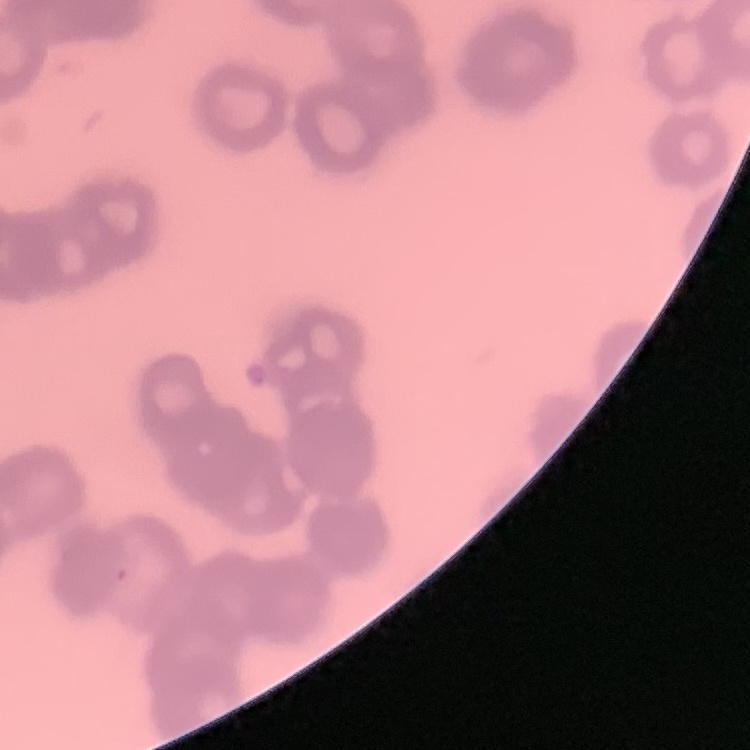

{
  "erythrocyte_morphology": "rouleaux formation",
  "preparation": "thin blood film",
  "stain": "Field's or Giemsa",
  "image_type": "one tile cut from a larger photomicrograph"
}